Name the cell type shown.
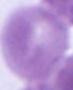

An erythrocyte.

1000x magnification. Micrograph.